Give the extent of all Babesia divergens-infected red blood cells.
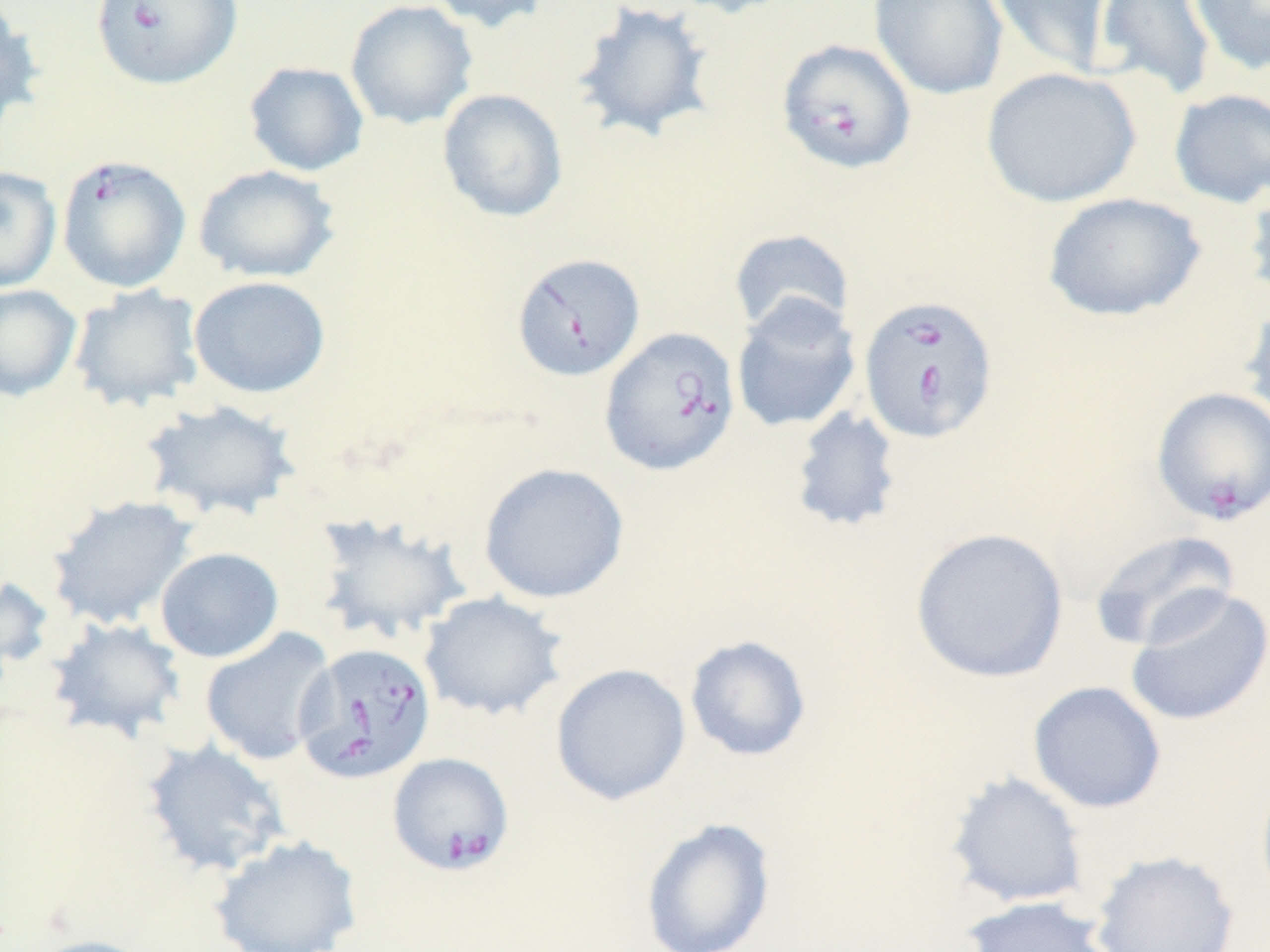
Approximate bounding boxes as (x1, y1, x2, y2) in pixels.
Babesia divergens-infected red blood cells: (89, 0, 242, 90), (776, 38, 916, 175), (56, 154, 191, 294), (511, 252, 646, 382), (857, 294, 999, 444), (598, 326, 741, 477), (1152, 386, 1270, 526), (294, 642, 437, 784), (387, 753, 514, 875).

{
  "slide_level_diagnosis": "Babesia divergens",
  "modality": "optical microscopy",
  "image_size": "1270×952 pixels",
  "stain": "May-Grünwald-Giemsa",
  "preparation": "thin blood film",
  "magnification": "1000x",
  "uninfected_red_blood_cell_locations": "approximate bounding boxes as (x1, y1, x2, y2) in pixels: (344, 0, 478, 130), (424, 0, 553, 34), (571, 0, 719, 145), (661, 0, 795, 18), (868, 0, 1009, 101), (987, 0, 1113, 78), (1094, 0, 1218, 101), (1188, 0, 1270, 76), (0, 4, 46, 131), (243, 61, 369, 177), (980, 66, 1141, 208), (1168, 87, 1270, 208), (437, 88, 569, 222), (193, 165, 340, 283), (0, 167, 62, 292), (1242, 173, 1270, 310), (1042, 192, 1206, 322), (728, 229, 854, 337), (188, 276, 331, 399), (0, 284, 82, 401), (68, 285, 206, 412), (731, 294, 862, 434), (1239, 299, 1270, 432), (140, 398, 302, 522), (788, 407, 905, 534), (477, 462, 630, 604), (45, 494, 199, 630), (309, 512, 472, 645), (910, 527, 1069, 684), (1089, 529, 1240, 651), (154, 547, 284, 663), (0, 575, 56, 679), (1125, 585, 1270, 727), (419, 591, 568, 720), (46, 618, 187, 743), (199, 627, 336, 766), (684, 635, 812, 762), (550, 663, 691, 806), (1027, 680, 1167, 814), (141, 738, 290, 879), (944, 771, 1090, 909), (1255, 771, 1270, 908), (640, 817, 777, 952), (208, 834, 364, 952), (1090, 849, 1240, 952), (961, 895, 1118, 952), (23, 935, 160, 952)",
  "field_of_view": "single"
}